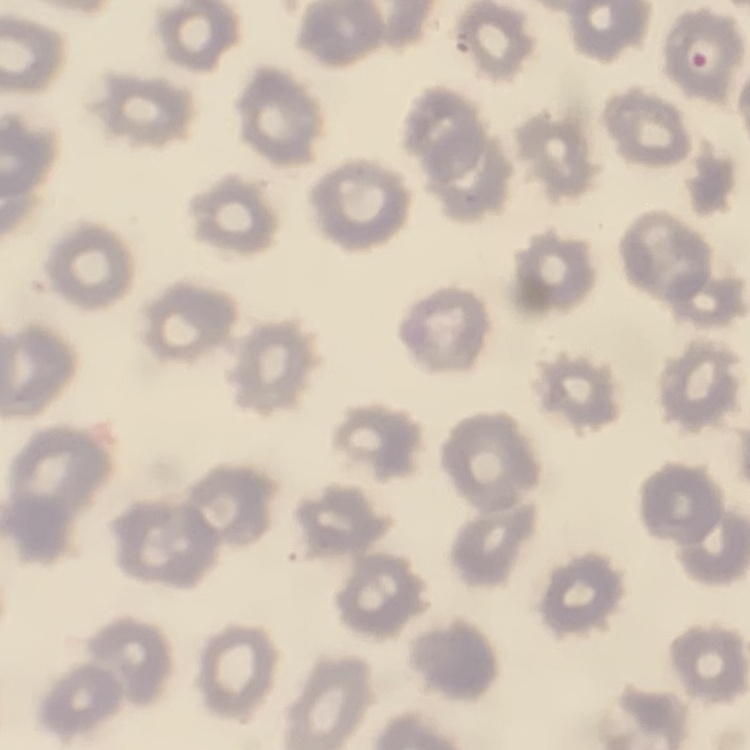

Summary:
  - Erythrocyte morphology: no rouleaux formation
  - Preparation: thin peripheral smear
  - Stain: Field's or Giemsa
  - Image type: square crop of a larger photomicrograph